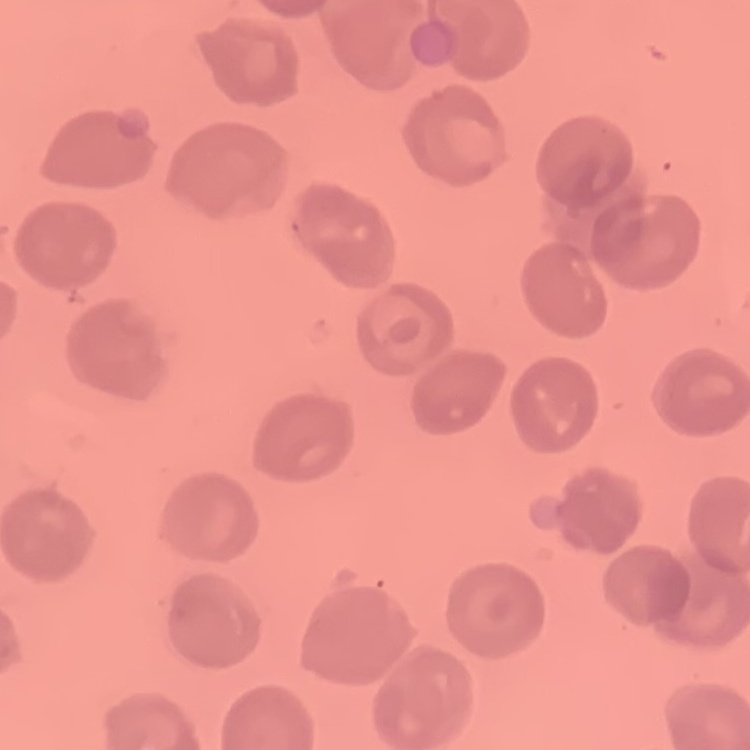

erythrocyte morphology = no rouleaux formation
stain = Field's or Giemsa
image type = square crop of a larger photomicrograph
preparation = thin blood smear